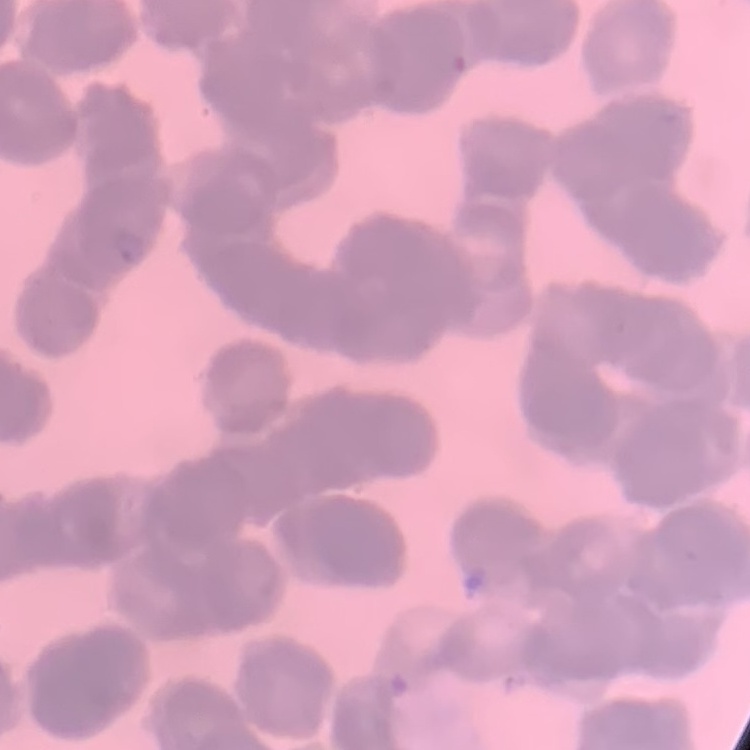
Summary:
  - Erythrocyte morphology: rouleaux formation
  - Stain: Field's or Giemsa
  - Preparation: thin blood smear
  - Image type: square crop of a larger photomicrograph